Identify the blood parasite species.
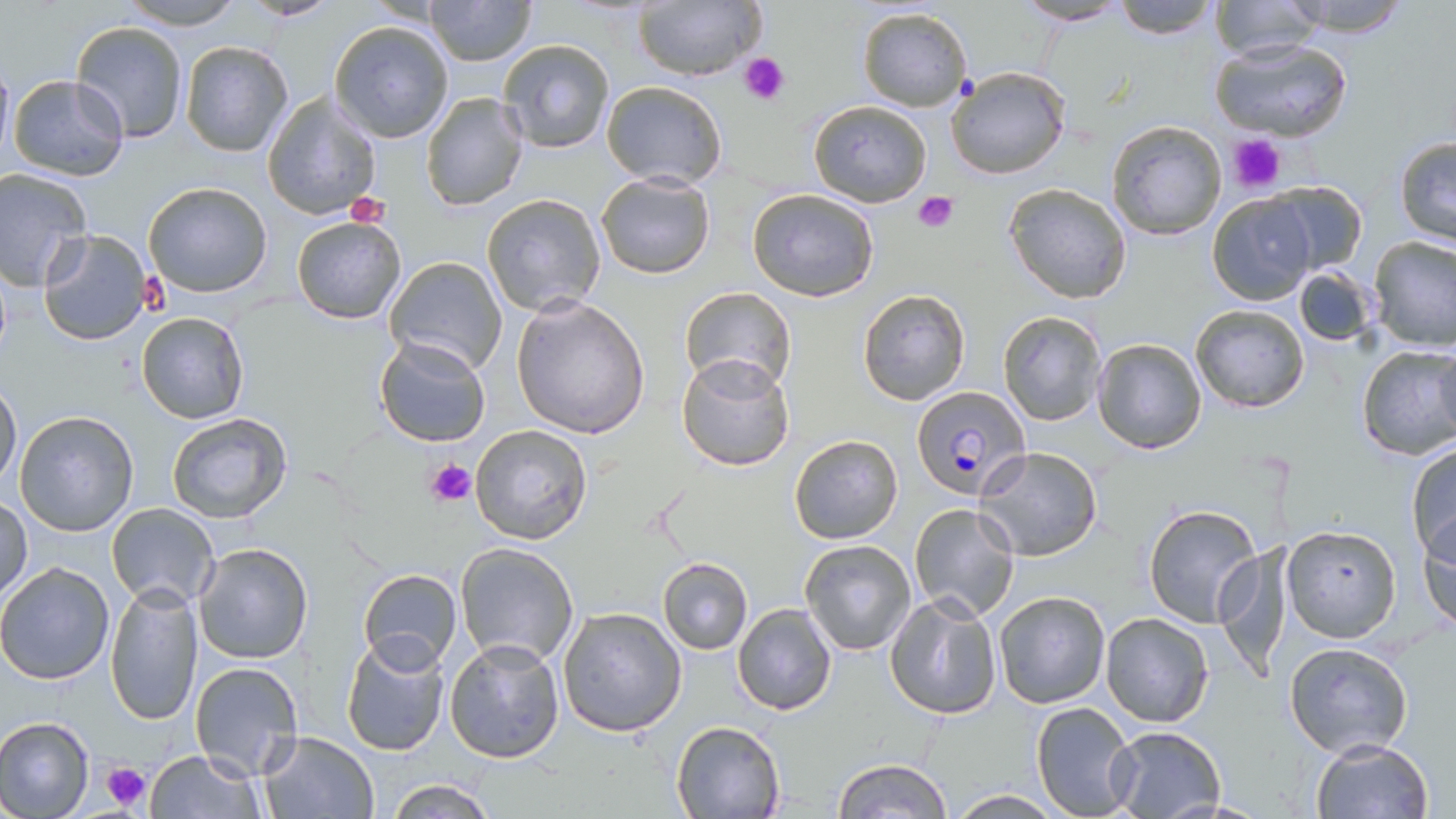
Plasmodium falciparum.

image_size: 1456×819 pixels
stain: May-Grünwald-Giemsa
plasmodium_falciparum_infected_red_blood_cell_locations: 'approximate bounding boxes as (x1, y1, x2, y2) in pixels: (910, 384, 1030, 500)'
magnification: 1000x
platelet_locations: 'approximate bounding boxes as (x1, y1, x2, y2) in pixels: (740, 53, 789, 105), (1227, 132, 1287, 193), (914, 192, 958, 233), (142, 273, 172, 317), (424, 456, 477, 509), (99, 760, 153, 810)'
modality: optical microscopy
preparation: thin blood smear
field_of_view: single
uninfected_red_blood_cell_locations: 'approximate bounding boxes as (x1, y1, x2, y2) in pixels: (120, 0, 245, 30), (424, 0, 535, 66), (633, 0, 764, 81), (1110, 0, 1220, 38), (1275, 0, 1417, 36), (1016, 1, 1131, 26), (1208, 1, 1325, 64), (857, 5, 973, 112), (329, 20, 455, 143), (71, 21, 190, 142), (498, 38, 615, 153), (1209, 39, 1353, 141), (180, 40, 293, 158), (945, 65, 1073, 180), (6, 73, 128, 182), (600, 80, 727, 188), (419, 91, 529, 211), (262, 92, 380, 221), (806, 98, 933, 207), (1104, 120, 1227, 241), (1393, 136, 1456, 246), (0, 167, 93, 291), (597, 172, 716, 279), (142, 182, 273, 298), (1266, 182, 1367, 272), (1004, 183, 1130, 302), (746, 188, 878, 301), (481, 192, 607, 318), (1206, 193, 1316, 305), (291, 215, 406, 324), (36, 228, 154, 347), (1368, 235, 1456, 351), (382, 254, 508, 375), (1291, 265, 1377, 348), (680, 287, 795, 393), (857, 287, 971, 406), (511, 296, 651, 438), (1190, 305, 1309, 413), (997, 310, 1105, 426), (136, 312, 248, 424), (373, 335, 491, 448), (1092, 338, 1208, 454), (1433, 343, 1456, 444), (1355, 344, 1456, 461), (676, 352, 797, 473), (0, 380, 22, 486), (13, 411, 139, 537), (166, 413, 294, 526), (471, 424, 593, 545), (789, 434, 903, 544), (1405, 441, 1456, 563), (976, 446, 1103, 561), (0, 493, 32, 603), (1142, 502, 1264, 628), (105, 503, 220, 607), (908, 503, 1021, 622), (1416, 513, 1456, 630), (1280, 524, 1401, 642), (799, 539, 918, 656), (192, 541, 313, 665), (455, 541, 581, 667), (1213, 545, 1283, 682), (658, 559, 753, 653), (0, 561, 116, 684), (357, 568, 463, 670), (105, 582, 203, 727), (885, 589, 1001, 719), (991, 591, 1110, 709), (732, 604, 838, 716), (558, 606, 687, 736), (1100, 612, 1215, 728), (337, 629, 451, 756), (443, 635, 564, 763), (1284, 641, 1413, 758), (189, 661, 304, 783), (1030, 702, 1138, 819), (0, 716, 95, 818), (670, 720, 785, 817), (1106, 727, 1225, 816), (258, 731, 378, 818), (1310, 737, 1434, 819), (143, 749, 266, 819), (831, 758, 951, 819), (382, 779, 498, 817), (949, 789, 1062, 818)'